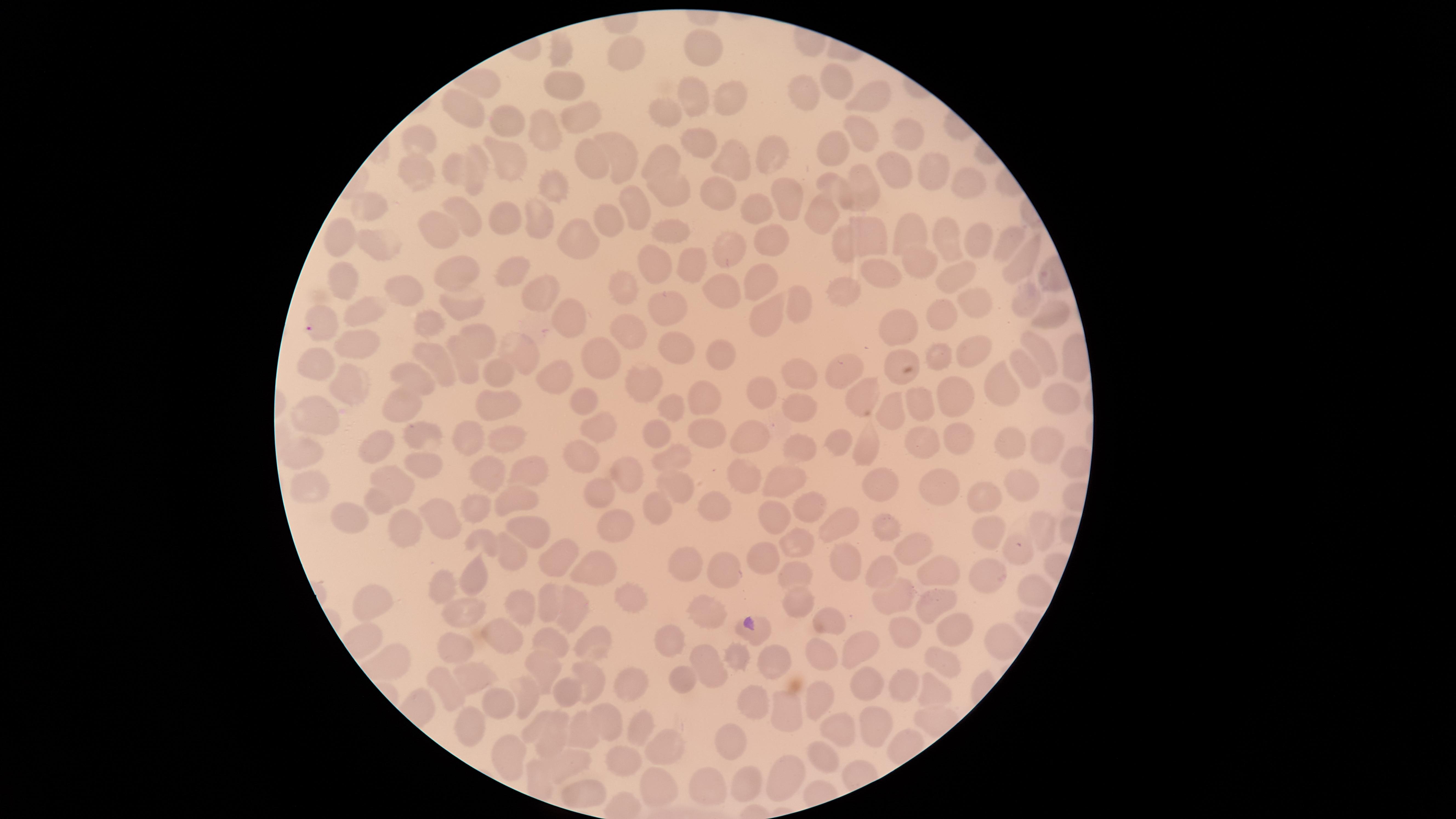
{
  "parasitized_red_blood_cells": "approximate marker points as [x, y] in pixels: [310, 330], [1020, 547]",
  "species": "Plasmodium falciparum",
  "stain": "Giemsa",
  "visible_region": "circular",
  "preparation": "thin blood smear",
  "field_of_view": "single",
  "image_size": "1456×819 pixels",
  "presence": "malaria parasites identified",
  "uninfected_red_blood_cells": "approximate marker points as [x, y] in pixels: [564, 48], [630, 53], [705, 53], [842, 83], [563, 84], [734, 99], [809, 99], [875, 102], [693, 103], [466, 108], [668, 113], [582, 116], [511, 124], [544, 127], [858, 134], [908, 135], [417, 141], [696, 143], [833, 149], [772, 155], [733, 157], [589, 158], [623, 158], [661, 163], [511, 165], [936, 167], [484, 171], [459, 172], [416, 175], [894, 176], [866, 184], [833, 185], [970, 185], [554, 191], [674, 192], [716, 194], [782, 196], [371, 205], [747, 209], [639, 210], [465, 212], [826, 213], [608, 217], [505, 221], [541, 223], [672, 229], [913, 232], [435, 236], [950, 236], [331, 238], [580, 240], [873, 240], [1010, 240], [767, 242], [982, 242], [374, 245], [841, 247], [729, 248], [660, 261], [693, 261], [1022, 265], [924, 266], [517, 272], [453, 273], [880, 274], [960, 278], [343, 279], [761, 281], [400, 282], [843, 286], [628, 290], [533, 293], [724, 296], [1026, 299], [672, 302], [798, 302], [972, 306], [457, 308], [363, 316], [762, 316], [1048, 316], [565, 317], [941, 317], [424, 319], [899, 326], [631, 331], [479, 339], [357, 344], [680, 345], [520, 350], [1043, 350], [973, 351], [604, 354], [723, 355], [939, 356], [899, 360], [440, 364], [323, 365], [467, 367], [498, 370], [800, 371], [1028, 373], [561, 374], [417, 380], [845, 381], [348, 382], [644, 382], [1004, 389], [953, 392], [761, 394], [865, 394], [583, 396], [1057, 397], [708, 400], [921, 401], [895, 404], [501, 406], [673, 406], [803, 409], [408, 411], [321, 416], [599, 425], [754, 433], [707, 434], [652, 435], [417, 437], [465, 437], [514, 438], [964, 441], [839, 445], [1011, 445], [869, 446], [921, 446], [803, 448], [379, 449], [1047, 449], [299, 451], [672, 457], [585, 458], [429, 466], [529, 468], [485, 473], [625, 474], [744, 475], [393, 478], [785, 480], [1029, 485], [672, 490], [311, 491], [944, 491], [595, 493], [880, 493], [989, 498], [380, 501], [523, 501], [721, 505], [810, 506], [478, 508], [659, 509], [355, 516], [610, 520], [774, 520], [444, 522], [844, 524], [882, 527], [526, 528], [1042, 532], [992, 533], [408, 534], [800, 538], [484, 542], [908, 545], [553, 554], [761, 555], [512, 556], [690, 566], [595, 570], [474, 571], [844, 571], [725, 572], [787, 574], [934, 575], [881, 576], [988, 576], [442, 587], [1035, 591], [633, 598], [518, 602], [377, 603], [802, 603], [901, 604], [547, 606], [572, 607], [936, 608], [708, 614], [462, 620], [827, 625], [766, 635], [956, 635], [494, 636], [903, 636], [997, 639], [671, 640], [555, 644], [588, 646], [860, 650], [452, 652], [821, 654], [737, 658], [776, 663], [545, 664], [947, 664], [711, 666], [589, 674], [476, 678], [630, 678], [683, 680], [906, 683], [865, 685], [447, 689], [939, 690], [569, 693], [524, 698], [751, 699], [820, 701], [498, 704], [792, 706], [610, 718], [537, 724], [879, 724], [471, 725], [643, 729], [838, 730], [589, 731], [555, 734], [732, 742], [663, 747], [506, 752], [823, 758], [626, 760], [568, 765], [788, 777], [748, 781], [713, 784], [657, 786], [584, 796]",
  "capture": "smartphone photograph through the microscope eyepiece"
}